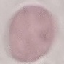
Summary:
  - Malaria status: uninfected
  - Stain: Giemsa
  - Image type: automatically extracted cell patch, resized to 64 × 64 pixels
  - Preparation: thin smear
  - Capture: smartphone through the microscope eyepiece